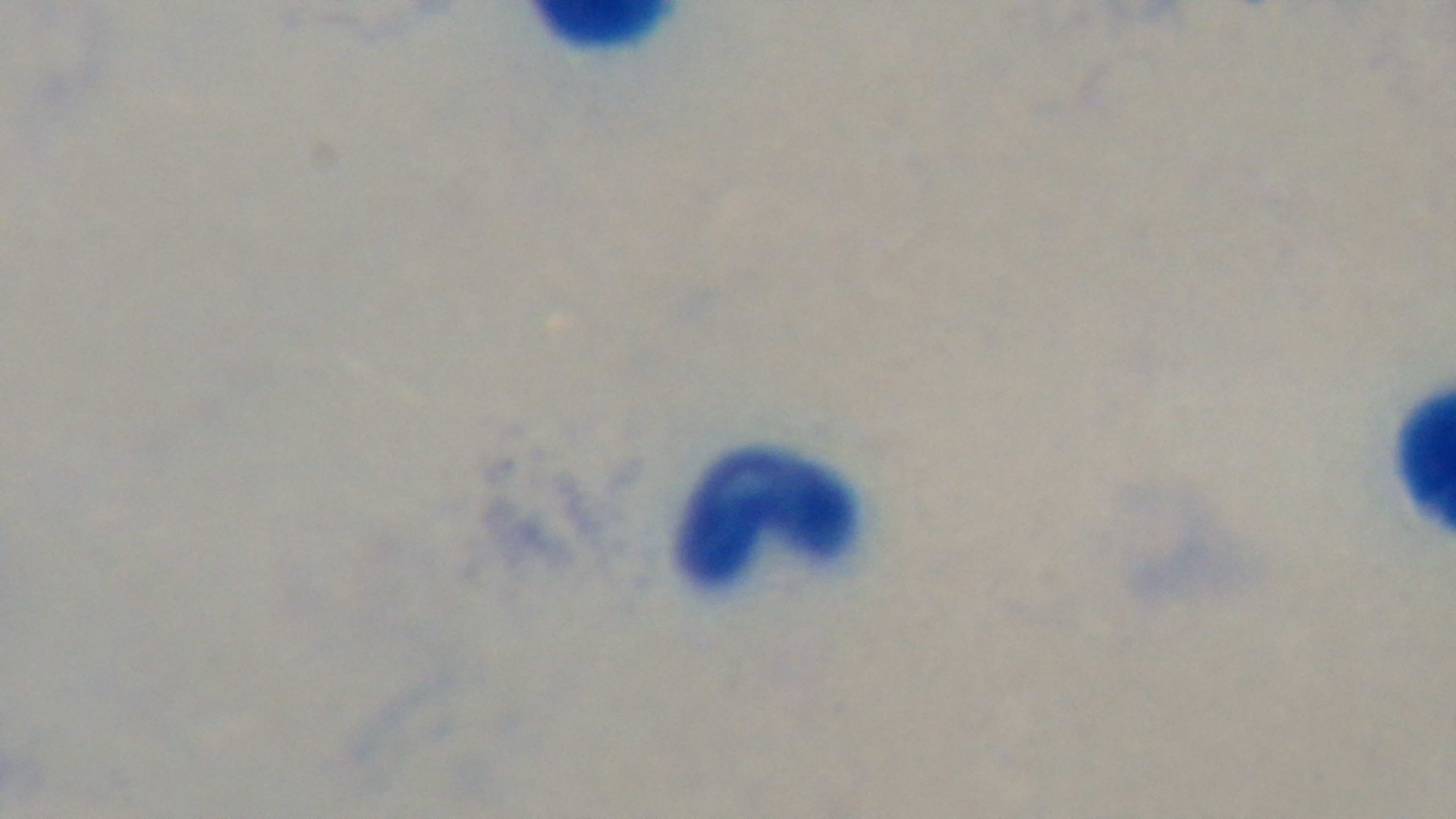
Summary:
  - Preparation: thick
  - Malaria status: uninfected
  - Modality: light microscopy
  - Stain: Giemsa
  - Objective: 100x oil immersion
  - Capture: mounted 4K digital camera
  - Field of view: single